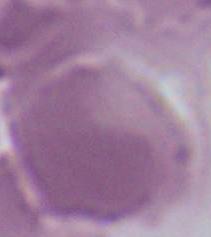

{
  "magnification": "1000x",
  "modality": "micrograph",
  "identification": "red blood cell"
}